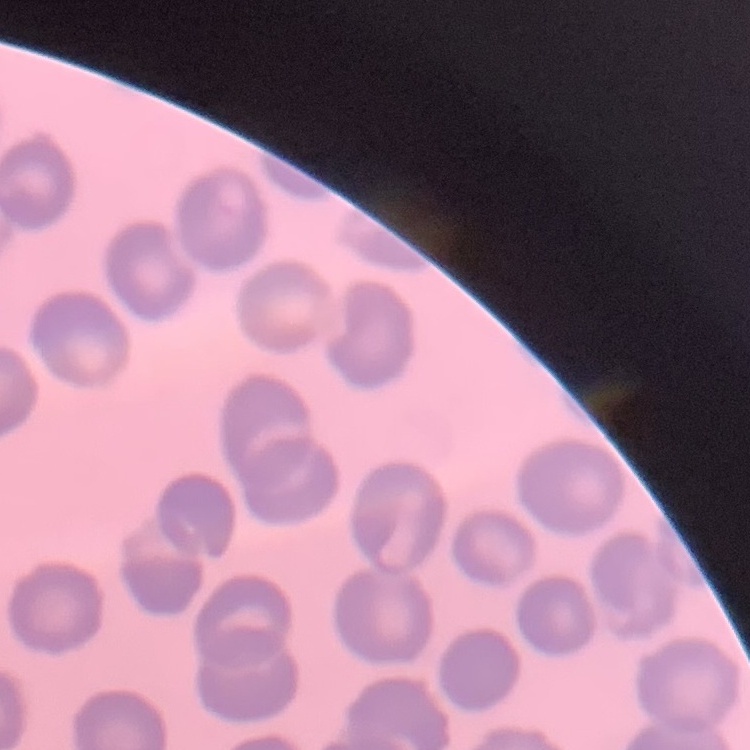 The erythrocytes show no rouleaux formation. Square crop of a larger photomicrograph. Thin blood smear. Stained with either Field's or Giemsa.